Report the malaria status of this cell.
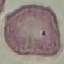
Uninfected.

image type = automatically extracted cell patch, resized to 64 × 64 pixels
preparation = thin blood smear
stain = Giemsa
capture = smartphone camera at the microscope eyepiece